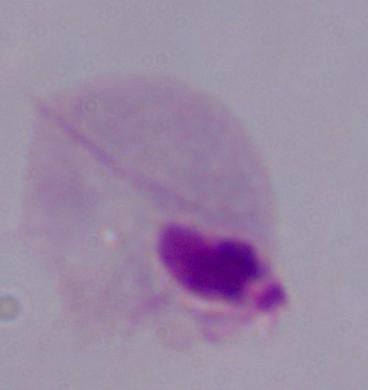

{
  "identification": "trichomonad",
  "magnification": "1000x",
  "modality": "photomicrograph"
}